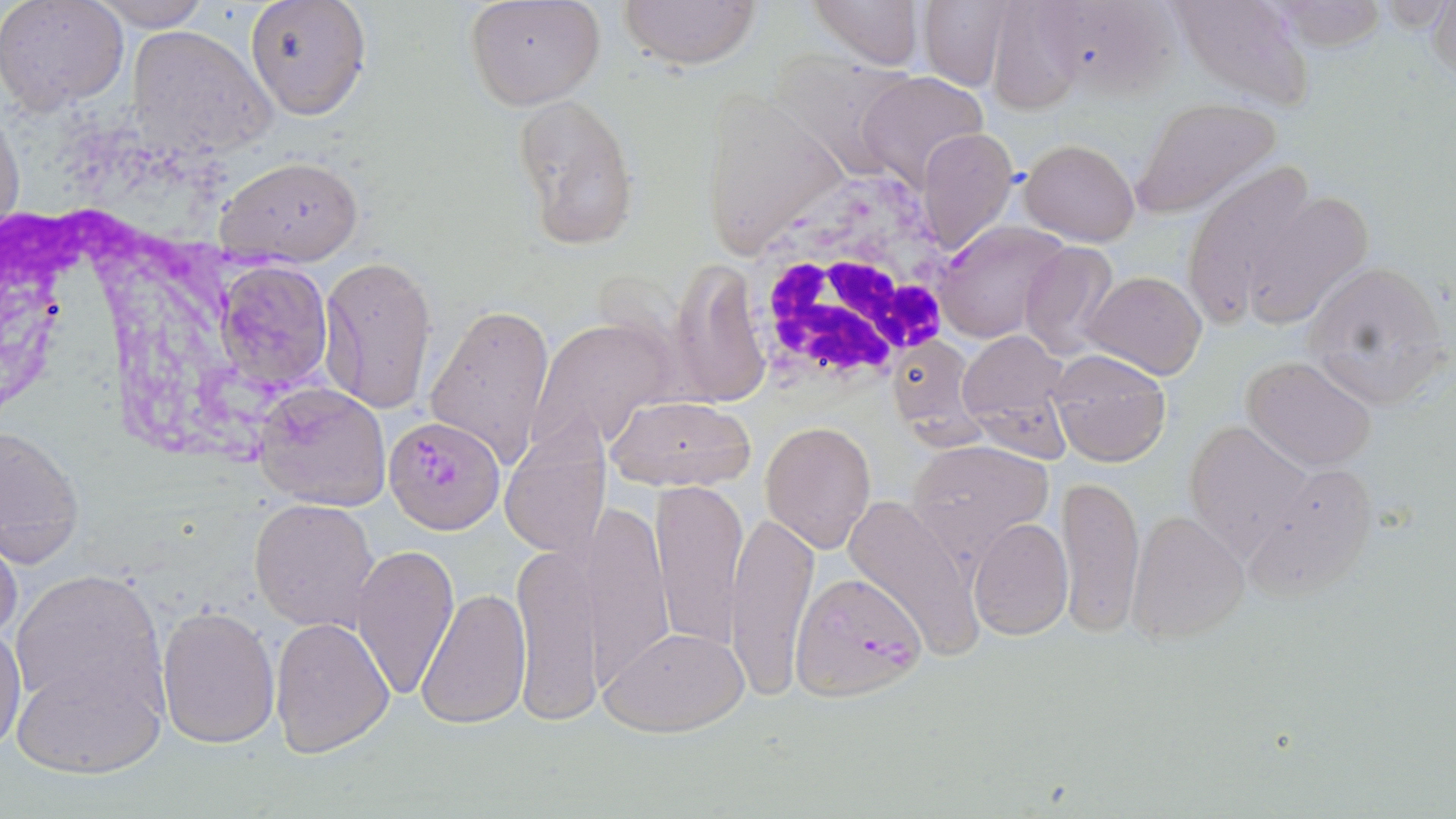
Summary:
  - Coordinate format: approximate bounding boxes as named x1/y1/x2/y2 corners in pixels
  - Plasmodium falciparum-infected red blood cell locations: (x1=935, y1=220, x2=1071, y2=342), (x1=388, y1=418, x2=508, y2=538), (x1=792, y1=571, x2=926, y2=702)
  - Uninfected red blood cell locations: (x1=0, y1=0, x2=131, y2=113), (x1=464, y1=0, x2=605, y2=111), (x1=618, y1=0, x2=763, y2=69), (x1=810, y1=0, x2=927, y2=70), (x1=1030, y1=0, x2=1185, y2=100), (x1=1169, y1=0, x2=1316, y2=113), (x1=1261, y1=0, x2=1392, y2=51), (x1=1426, y1=0, x2=1455, y2=85), (x1=89, y1=1, x2=211, y2=31), (x1=246, y1=1, x2=371, y2=121), (x1=915, y1=1, x2=1013, y2=89), (x1=979, y1=2, x2=1095, y2=111), (x1=125, y1=25, x2=274, y2=161), (x1=782, y1=58, x2=913, y2=172), (x1=856, y1=71, x2=989, y2=189), (x1=699, y1=88, x2=845, y2=258), (x1=511, y1=92, x2=640, y2=251), (x1=1132, y1=98, x2=1283, y2=217), (x1=0, y1=102, x2=23, y2=246), (x1=918, y1=128, x2=1017, y2=253), (x1=1020, y1=138, x2=1140, y2=246), (x1=215, y1=153, x2=365, y2=263), (x1=1184, y1=161, x2=1320, y2=324), (x1=1236, y1=187, x2=1372, y2=328), (x1=1019, y1=241, x2=1121, y2=360), (x1=318, y1=254, x2=437, y2=414), (x1=217, y1=258, x2=335, y2=393), (x1=1300, y1=258, x2=1452, y2=410), (x1=1083, y1=270, x2=1206, y2=381), (x1=425, y1=300, x2=557, y2=467), (x1=525, y1=316, x2=677, y2=456), (x1=957, y1=329, x2=1069, y2=451), (x1=886, y1=337, x2=981, y2=440), (x1=1047, y1=348, x2=1173, y2=466), (x1=1241, y1=355, x2=1378, y2=472), (x1=253, y1=382, x2=392, y2=513), (x1=602, y1=394, x2=759, y2=492), (x1=760, y1=420, x2=877, y2=555), (x1=0, y1=421, x2=86, y2=566), (x1=1183, y1=421, x2=1314, y2=559), (x1=500, y1=425, x2=612, y2=561), (x1=906, y1=439, x2=1055, y2=559), (x1=1247, y1=461, x2=1381, y2=600), (x1=1057, y1=472, x2=1145, y2=636), (x1=651, y1=479, x2=748, y2=651), (x1=843, y1=490, x2=984, y2=662), (x1=250, y1=497, x2=381, y2=632), (x1=585, y1=504, x2=676, y2=691), (x1=728, y1=507, x2=818, y2=695), (x1=1126, y1=511, x2=1249, y2=645), (x1=969, y1=518, x2=1074, y2=639), (x1=0, y1=526, x2=23, y2=651), (x1=511, y1=541, x2=603, y2=726), (x1=352, y1=542, x2=458, y2=699), (x1=9, y1=569, x2=166, y2=716), (x1=417, y1=585, x2=531, y2=729), (x1=155, y1=602, x2=280, y2=748), (x1=270, y1=618, x2=395, y2=760), (x1=0, y1=619, x2=26, y2=757), (x1=602, y1=625, x2=750, y2=738), (x1=10, y1=653, x2=165, y2=780)
  - White blood cell locations: (x1=735, y1=170, x2=967, y2=398)
  - Slide-level diagnosis: Plasmodium falciparum
  - Preparation: thin blood film
  - Image size: 1456×819 pixels
  - Magnification: 1000x
  - Modality: optical microscopy
  - Field of view: single
  - Stain: May-Grünwald-Giemsa